Point out every malaria parasite.
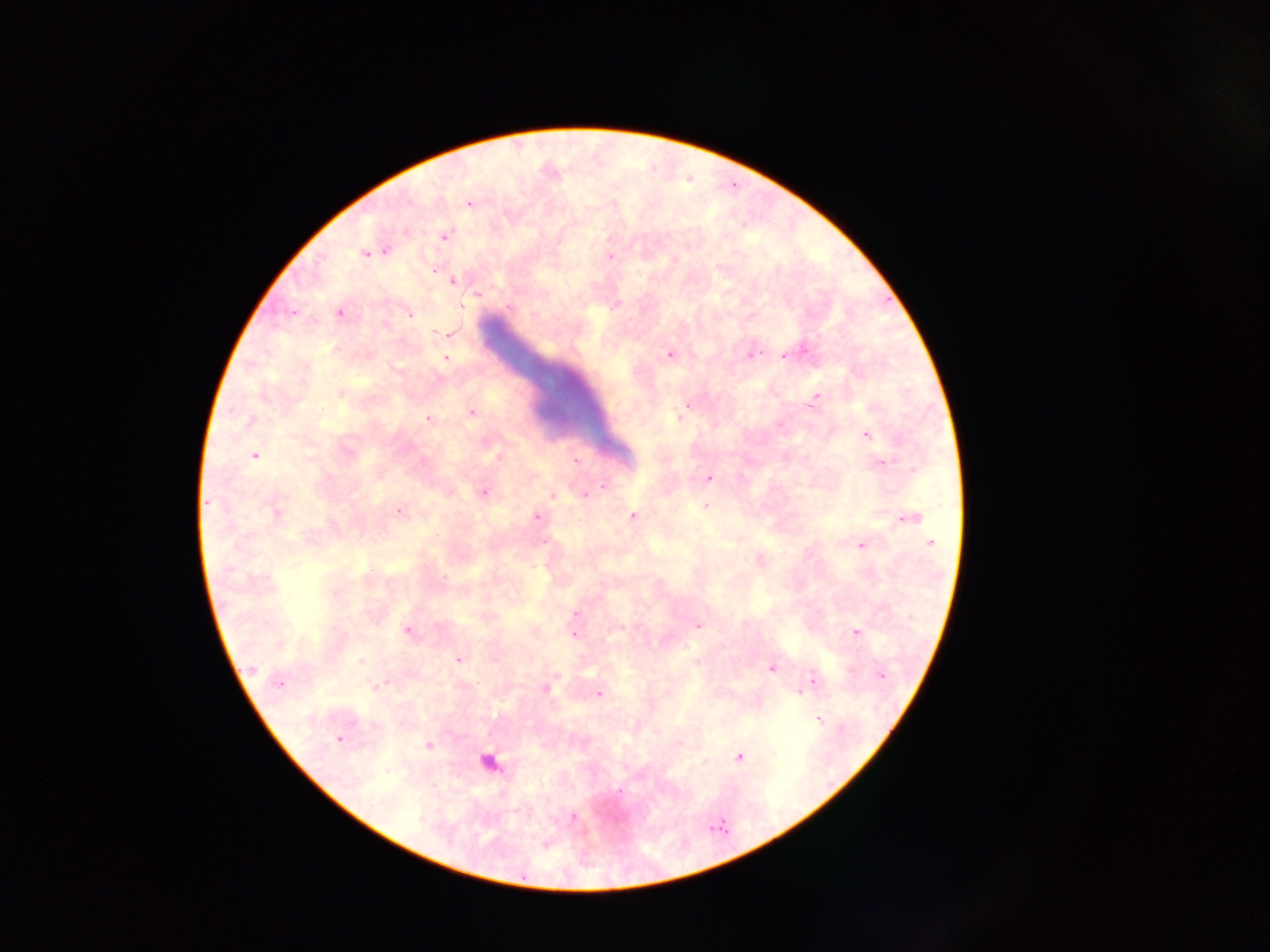

Approximate centers as (x, y) in pixels.
Malaria parasites: (469, 203), (445, 235), (365, 255), (610, 256), (453, 281), (463, 305), (340, 312), (407, 314), (292, 316), (450, 335), (805, 352), (671, 354), (750, 354), (781, 356), (446, 359), (816, 397), (471, 410), (427, 417), (867, 435), (255, 455), (575, 460), (882, 461), (708, 479), (603, 485), (484, 494), (552, 494), (584, 495), (208, 505), (706, 505), (398, 511), (535, 516), (632, 516), (910, 518), (542, 541), (930, 542), (863, 545), (444, 578), (574, 615), (698, 625), (573, 626), (407, 631), (853, 631), (576, 633), (458, 659), (361, 661), (772, 668), (556, 676), (880, 676), (813, 679), (278, 683), (383, 683), (799, 693), (599, 694), (818, 720), (337, 740), (739, 757), (620, 788), (572, 817), (542, 845).

Leukocyte locations: (493, 767). Thick blood film. Collected in Ghana. Photographed through a microscope with a mobile-phone camera. One field of view. Image is 1270×952 pixels.